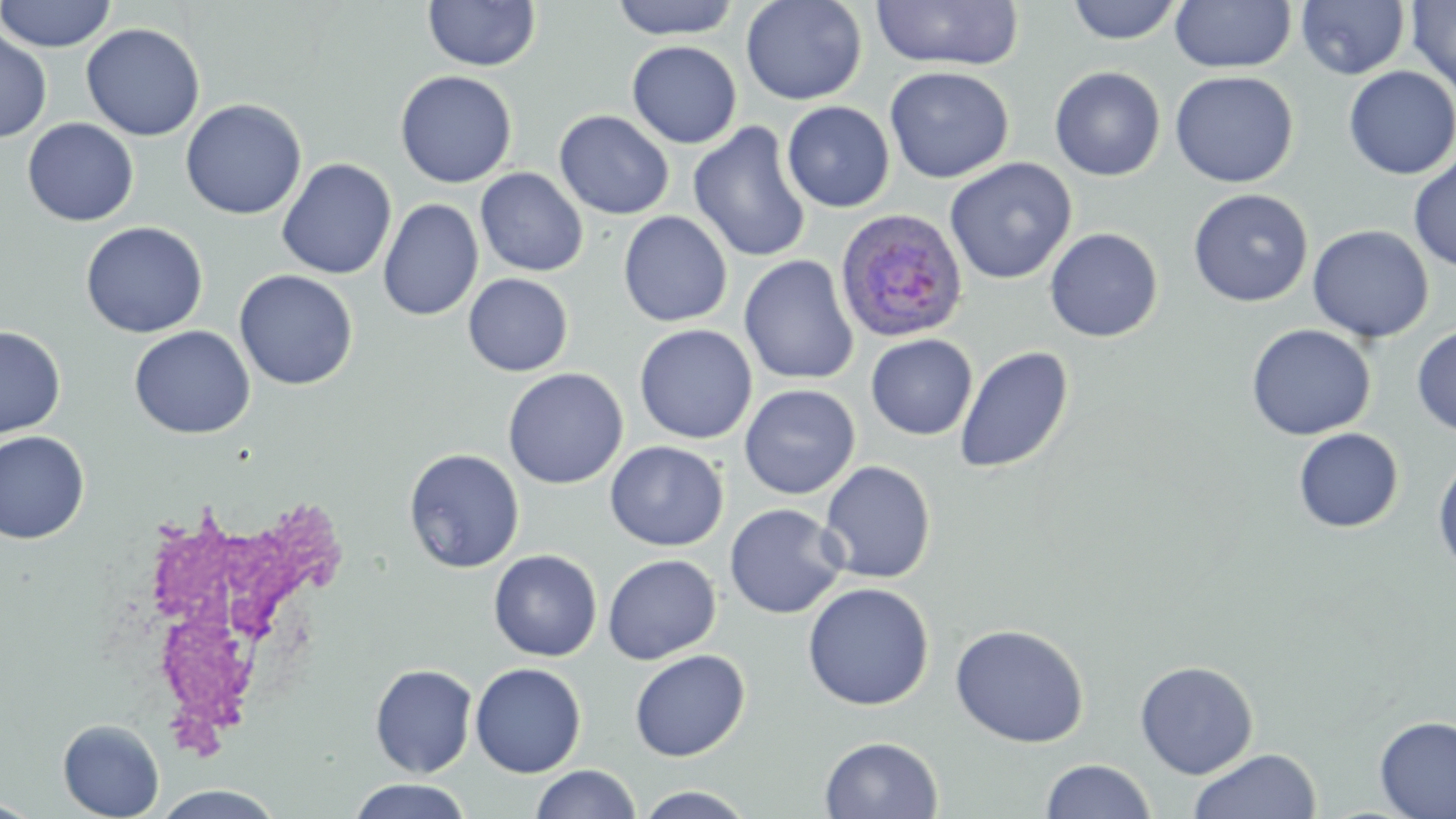
Summary:
  - Coordinate format: approximate bounding boxes as (x1,y1)-(x2,y2) corner pairs in pixels
  - Uninfected red blood cell locations: (0,0)-(117,52), (423,0)-(542,72), (609,0)-(741,40), (740,0)-(867,105), (1066,0)-(1184,44), (1170,0)-(1297,73), (1406,0)-(1456,97), (869,1)-(1023,70), (1296,1)-(1410,79), (81,23)-(205,141), (0,28)-(52,143), (626,41)-(742,149), (884,66)-(1014,184), (1049,66)-(1166,181), (1343,66)-(1456,179), (394,70)-(518,189), (1169,71)-(1299,188), (180,98)-(307,220), (782,101)-(895,213), (554,110)-(674,220), (22,117)-(139,227), (688,122)-(812,264), (1408,152)-(1456,272), (944,157)-(1077,284), (276,158)-(397,280), (476,168)-(589,277), (1188,188)-(1314,307), (378,198)-(484,322), (618,211)-(733,327), (80,222)-(208,338), (1307,225)-(1434,343), (1044,227)-(1164,342), (738,255)-(859,385), (234,269)-(359,390), (463,273)-(573,376), (1246,323)-(1376,440), (634,324)-(757,444), (1412,324)-(1456,437), (0,325)-(66,439), (129,325)-(255,439), (865,334)-(977,440), (954,345)-(1074,475), (502,368)-(628,489), (739,383)-(860,500), (1293,427)-(1404,533), (0,430)-(90,543), (605,441)-(728,551), (403,447)-(525,573), (1432,451)-(1456,578), (819,460)-(936,584), (724,503)-(847,619), (488,549)-(602,662), (602,554)-(721,665), (802,582)-(934,711), (949,623)-(1090,748), (629,649)-(751,762), (1134,660)-(1258,779), (470,662)-(587,777), (369,663)-(478,777), (1373,715)-(1456,819), (58,718)-(164,819), (819,735)-(943,818), (1188,749)-(1321,819), (1040,759)-(1156,818), (530,765)-(641,819), (347,779)-(474,818), (151,785)-(288,819), (633,785)-(757,818), (0,796)-(44,818)
  - White blood cell locations: (122,490)-(349,754)
  - Plasmodium ovale-infected red blood cell locations: (834,209)-(968,344)
  - Slide-level diagnosis: Plasmodium ovale
  - Image size: 1456×819 pixels
  - Modality: optical microscopy
  - Field of view: single
  - Preparation: thin blood film
  - Magnification: 1000x
  - Stain: May-Grünwald-Giemsa